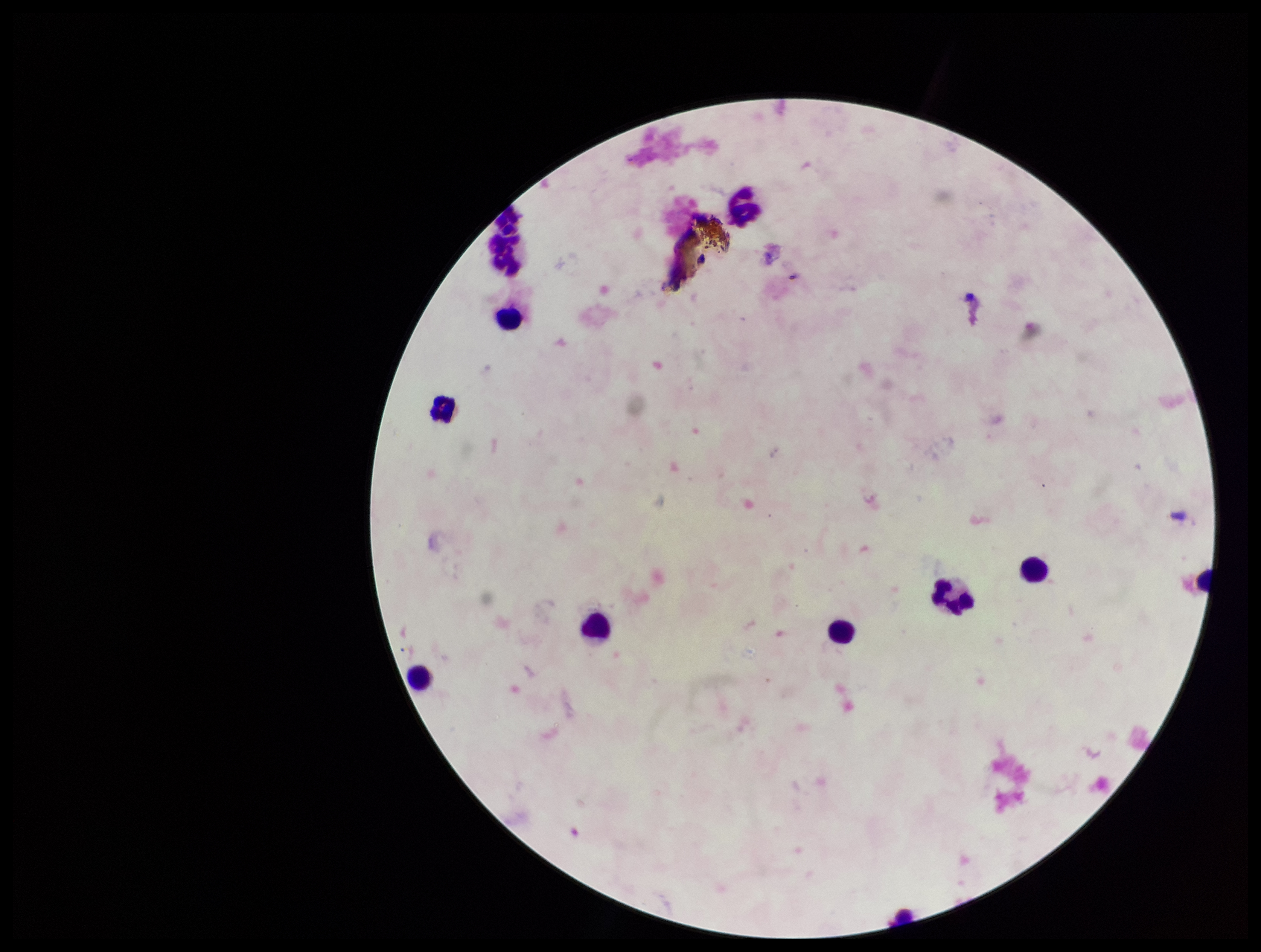
Summary:
  - Image size: 1261×952 pixels
  - Parasite count: 0
  - Preparation: thick
  - Plasmodium parasites: none detected
  - Patient malaria status: negative
  - Leukocyte count: 9
  - Stain: Giemsa
  - Field of view: single
  - Capture: smartphone photograph through the microscope eyepiece